Assess the morphology of the red blood cells.
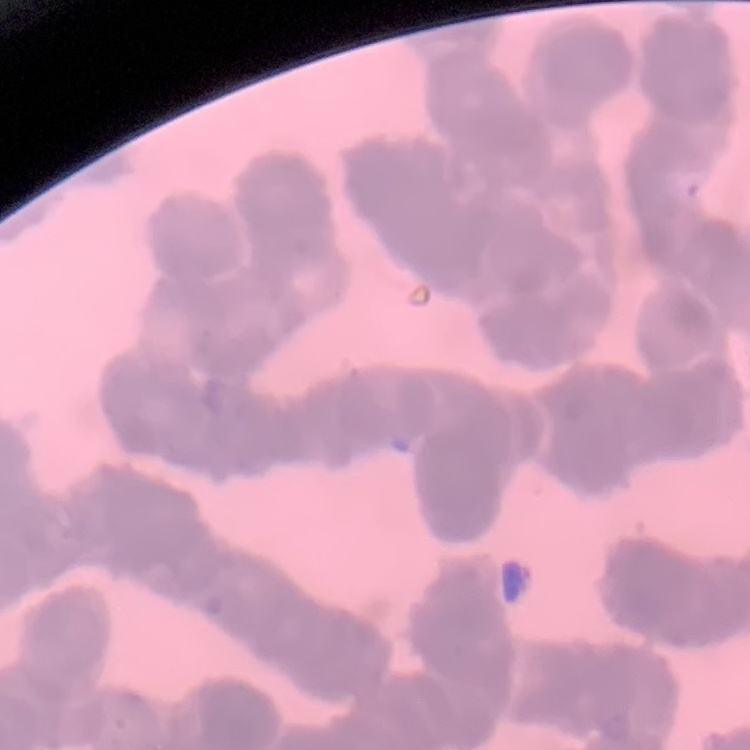
Rouleaux formation.

Stained with either Field's or Giemsa. One tile cut from a larger photomicrograph. Thin blood film.